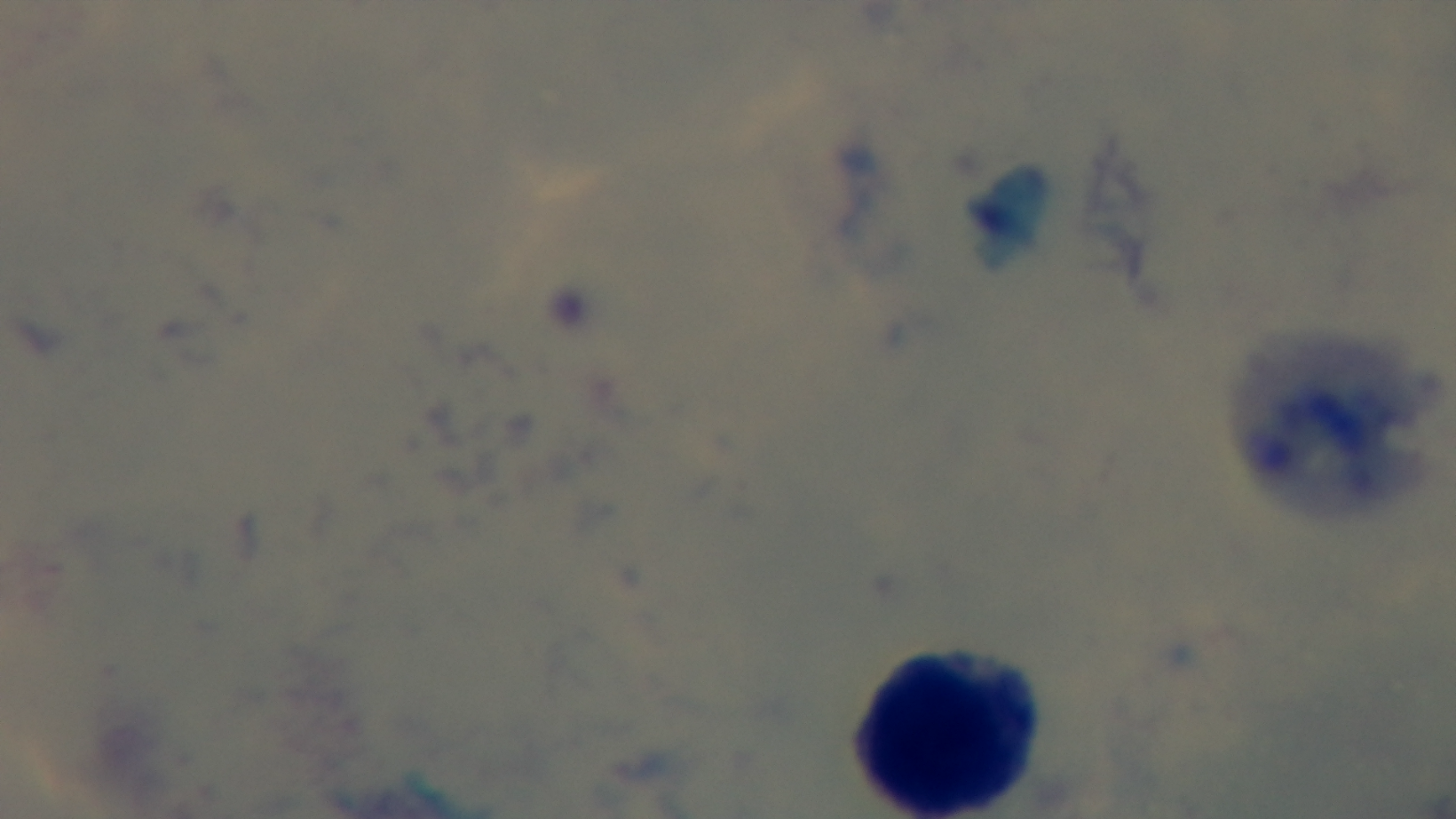
malaria status = negative
modality = light microscopy
stain = Giemsa
field of view = single
objective = 100x oil immersion
capture = mounted 4K digital camera
preparation = thick blood film